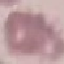
Summary:
  - Result: no malaria parasites detected
  - Stain: Giemsa
  - Preparation: thin smear
  - Image type: automatically extracted cell patch, resized to 64 × 64 pixels
  - Capture: smartphone through the microscope eyepiece